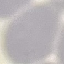

Result: no malaria parasites detected. Automatically extracted cell patch, resized to 64 × 64 pixels. Photographed with a smartphone camera at the microscope eyepiece. Thin blood smear. Giemsa-stained preparation.